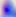
modality = photomicrograph
identification = Toxoplasma gondii
magnification = 400x